Classify this cell by malaria status.
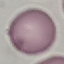

It is uninfected.

Photographed with a smartphone camera at the microscope eyepiece. Automatically extracted cell patch, resized to 64 × 64 pixels. Thin blood film. Giemsa-stained preparation.